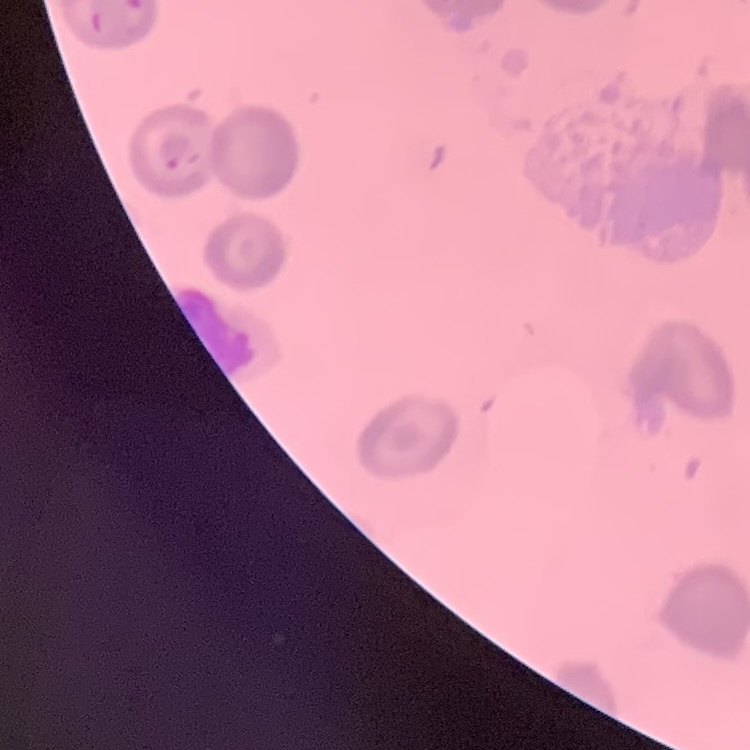
erythrocyte_morphology: no rouleaux formation
image_type: square crop of a larger photomicrograph
preparation: thin peripheral smear
stain: Field's or Giemsa